Mark where platelets are.
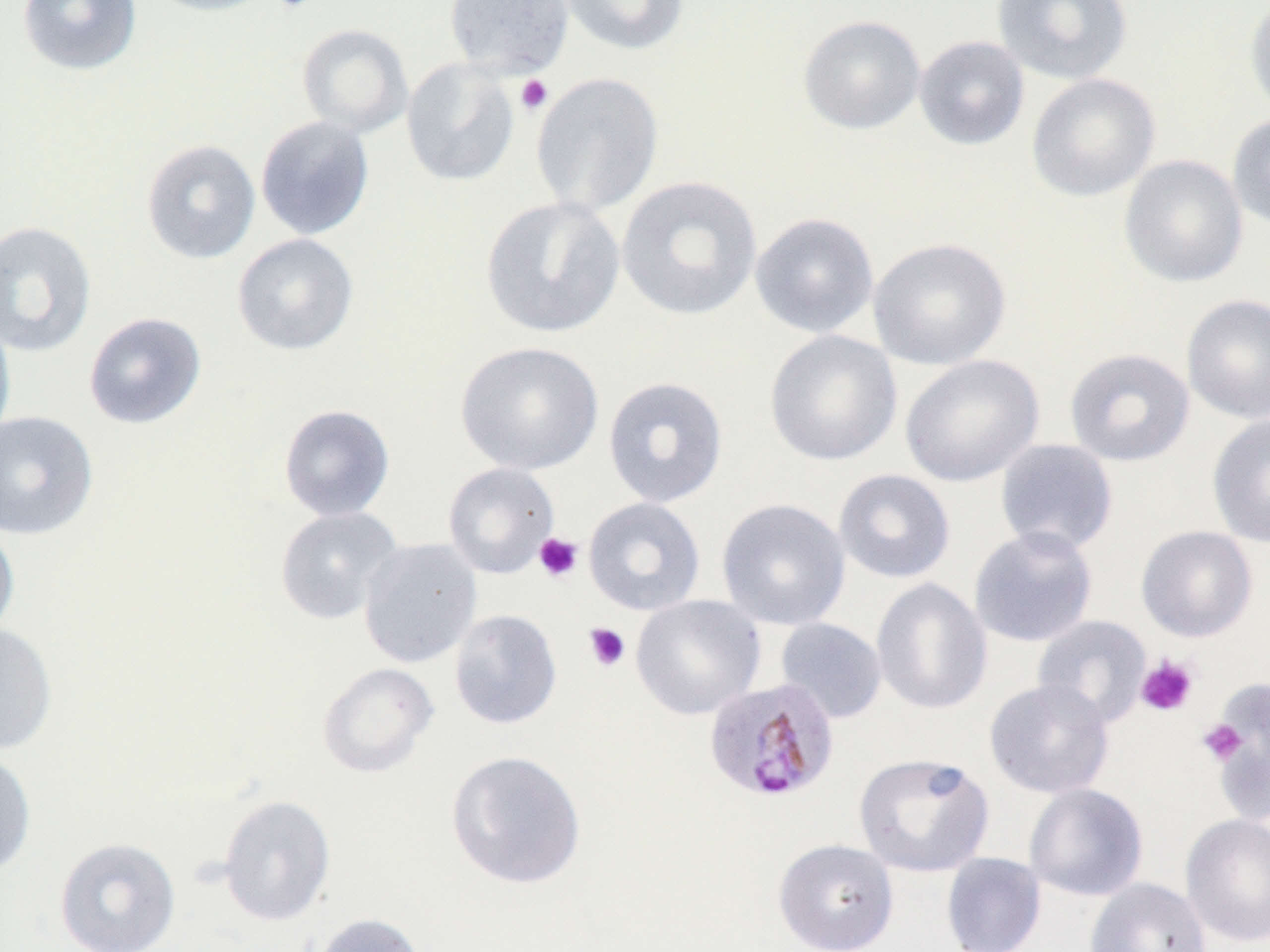
Approximate bounding boxes as (x1,y1)-(x2,y2) corner pairs in pixels.
Platelets: (271,0)-(318,13), (515,74)-(553,116), (533,532)-(584,583), (583,622)-(630,671), (1135,654)-(1199,717), (1198,718)-(1248,765).

Summary:
  - Plasmodium malariae-infected red blood cell locations: (703,677)-(839,802)
  - Uninfected red blood cell locations: (17,0)-(142,76), (142,0)-(278,17), (443,0)-(574,78), (554,0)-(689,56), (991,0)-(1133,85), (1244,0)-(1270,122), (798,15)-(926,135), (296,23)-(414,138), (913,35)-(1030,150), (401,58)-(520,187), (530,72)-(664,218), (1026,73)-(1160,202), (1226,113)-(1270,230), (255,115)-(375,240), (141,139)-(261,264), (1119,154)-(1249,288), (616,175)-(762,321), (480,196)-(625,338), (749,212)-(879,338), (0,220)-(97,358), (232,233)-(359,356), (868,237)-(1012,371), (1181,294)-(1270,424), (83,311)-(207,429), (0,312)-(16,450), (764,329)-(903,466), (455,341)-(604,475), (1064,348)-(1195,467), (900,354)-(1044,487), (602,376)-(729,508), (278,404)-(396,521), (0,410)-(99,539), (1207,413)-(1270,548), (995,439)-(1119,556), (442,462)-(560,578), (833,468)-(956,583), (583,497)-(706,616), (716,497)-(851,630), (274,505)-(404,625), (0,516)-(20,644), (968,525)-(1098,648), (1135,525)-(1258,642), (358,538)-(482,668), (871,577)-(992,715), (631,594)-(766,720), (449,609)-(562,730), (1032,615)-(1152,728), (774,617)-(888,724), (0,621)-(58,755), (316,662)-(439,778), (984,678)-(1114,799), (1201,690)-(1270,806), (0,748)-(37,877), (445,749)-(587,890), (853,752)-(994,877), (1023,783)-(1148,901), (217,794)-(336,926), (1180,813)-(1270,947), (54,837)-(181,952), (773,838)-(899,952), (941,852)-(1046,952), (1085,878)-(1211,952), (310,912)-(427,952)
  - Slide-level diagnosis: Plasmodium malariae
  - Magnification: 1000x
  - Preparation: thin blood smear
  - Field of view: single
  - Image size: 1270×952 pixels
  - Modality: optical microscopy
  - Stain: May-Grünwald-Giemsa